State the preparation type.
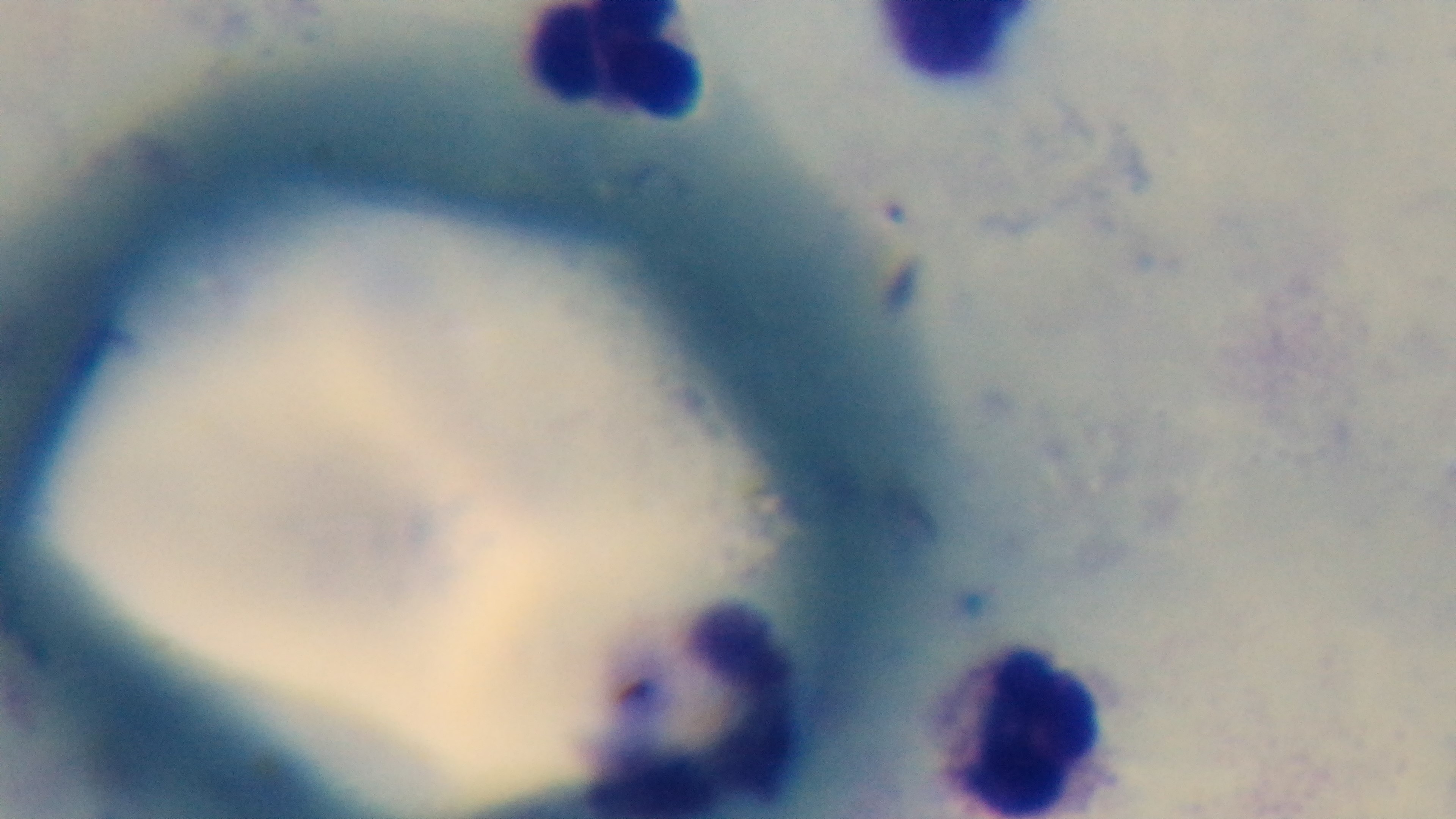
Thick.

Photomicrograph. Single field of view. Oil-immersion objective, 100x. Mounted 4K digital camera. Malaria status: negative. Giemsa stain.